Outline each Plasmodium ovale-infected red blood cell.
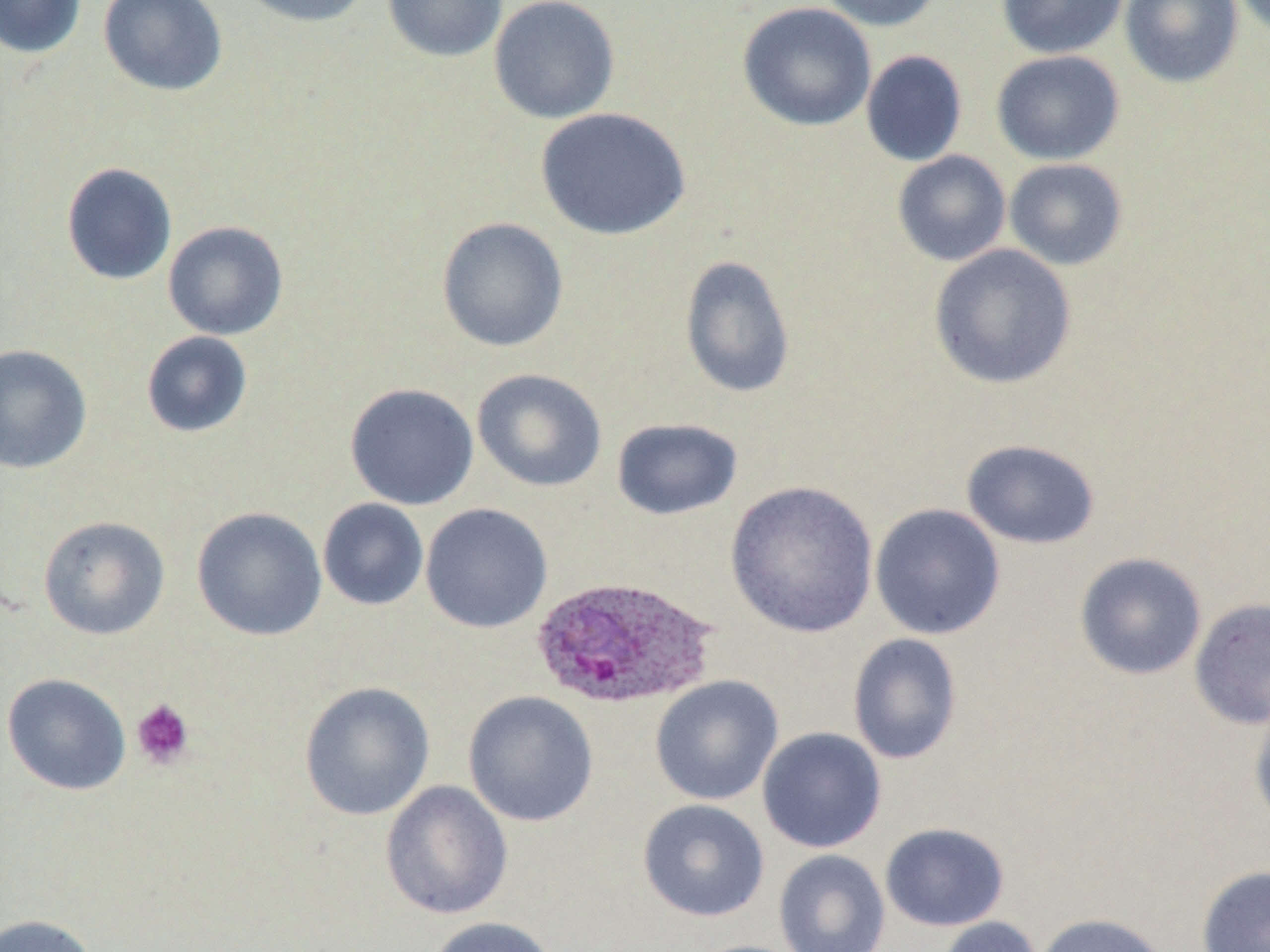
Approximate bounding boxes as (x1,y1)-(x2,y2) corner pairs in pixels.
Plasmodium ovale-infected red blood cells: (530,575)-(718,710).

{
  "slide_level_diagnosis": "Plasmodium ovale",
  "image_size": "1270×952 pixels",
  "field_of_view": "one of a larger specimen",
  "modality": "optical microscopy",
  "stain": "May-Grünwald-Giemsa",
  "uninfected_red_blood_cell_locations": "approximate bounding boxes as (x1,y1)-(x2,y2) corner pairs in pixels: (0,0)-(86,59), (98,0)-(228,97), (234,0)-(374,27), (382,0)-(507,62), (488,0)-(620,124), (815,0)-(946,32), (996,0)-(1130,59), (1119,0)-(1244,88), (737,2)-(877,132), (861,50)-(968,167), (990,50)-(1125,165), (535,107)-(691,241), (892,150)-(1012,267), (1004,158)-(1128,271), (60,162)-(177,286), (436,216)-(569,352), (163,221)-(288,340), (928,243)-(1078,390), (680,254)-(796,399), (141,331)-(253,438), (0,344)-(92,474), (471,368)-(607,492), (345,383)-(479,510), (611,418)-(742,521), (960,439)-(1101,549), (725,481)-(879,638), (317,498)-(429,611), (420,503)-(553,633), (869,503)-(1006,640), (191,506)-(327,641), (38,515)-(170,640), (1074,552)-(1208,680), (1189,598)-(1270,730), (847,633)-(963,765), (1,673)-(132,796), (650,675)-(783,806), (299,681)-(436,821), (463,690)-(599,827), (1249,702)-(1270,829), (757,727)-(887,853), (380,780)-(513,920), (637,799)-(770,922), (879,822)-(1009,931), (773,849)-(890,952), (1196,865)-(1270,952), (1034,912)-(1171,952), (0,914)-(99,952), (424,916)-(560,952), (936,916)-(1044,952)",
  "platelet_locations": "approximate bounding boxes as (x1,y1)-(x2,y2) corner pairs in pixels: (130,699)-(194,770)",
  "preparation": "thin blood film",
  "magnification": "1000x"
}